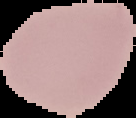
Malaria status: uninfected. From a thin blood film. The area outside the segmented cell region is set to black. Image is 136×118 pixels.